Classify this cell by malaria status.
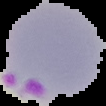

Parasitized.

Summary:
  - Image size: 106×106 pixels
  - Image type: segmented cell region with the area outside set to black
  - Preparation: thin blood film